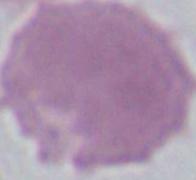

{
  "magnification": "1000x",
  "identification": "erythrocyte",
  "modality": "photomicrograph"
}